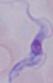
Photomicrograph. A trypanosome is seen. Captured at 1000x magnification.